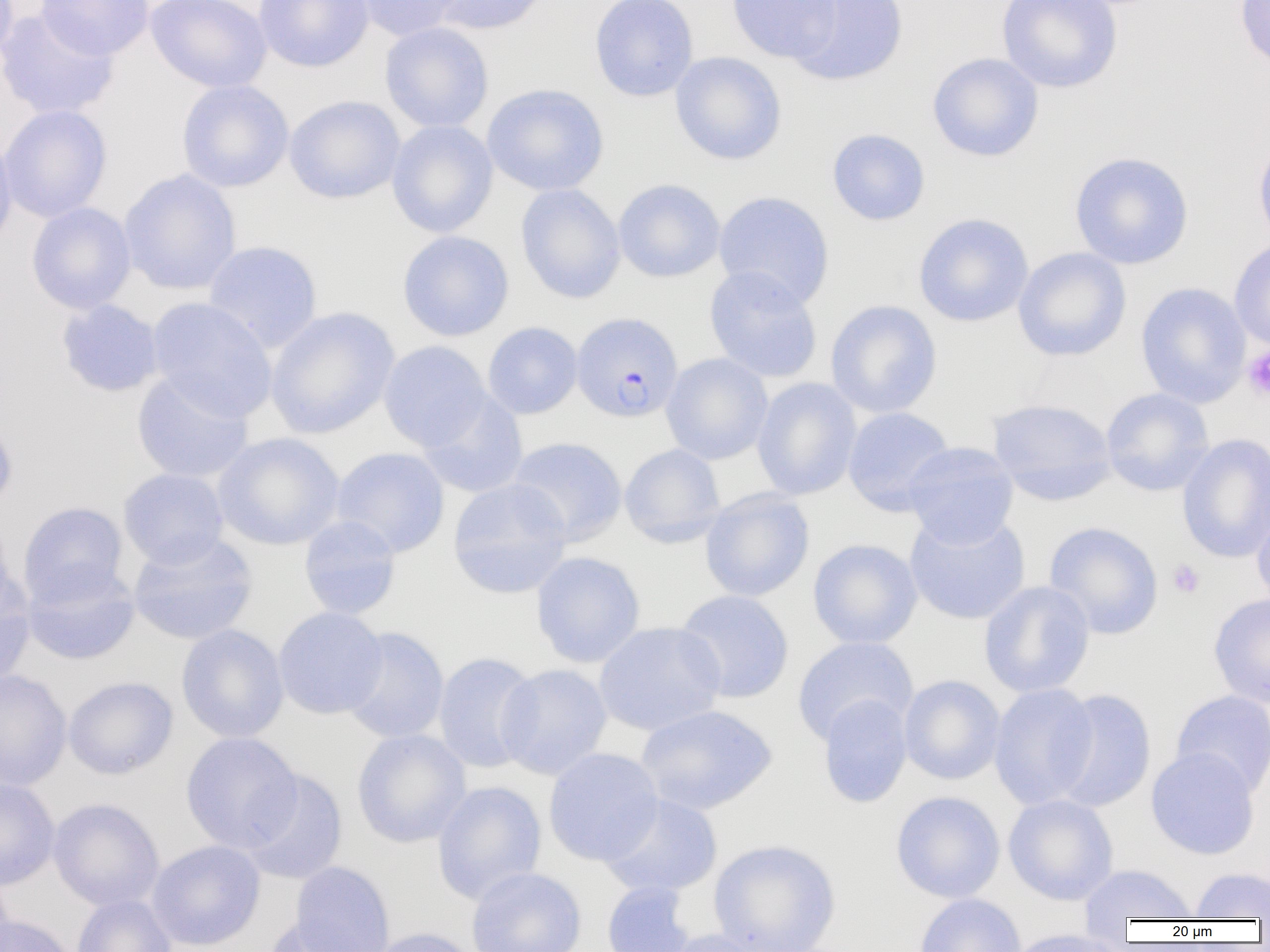
Summary:
  - Coordinate format: approximate bounding boxes as (x1, y1, x2, y2) in pixels
  - Plasmodium falciparum-infected red blood cell locations: (571, 312, 683, 422)
  - Uninfected red blood cell locations: (0, 0, 19, 72), (36, 0, 154, 60), (146, 0, 272, 92), (254, 0, 374, 72), (350, 0, 466, 41), (428, 0, 550, 35), (589, 0, 699, 101), (726, 0, 842, 64), (787, 0, 909, 87), (997, 0, 1123, 93), (1235, 0, 1270, 72), (0, 8, 120, 120), (379, 22, 494, 133), (670, 51, 787, 165), (927, 52, 1044, 162), (176, 80, 295, 192), (482, 83, 609, 196), (284, 95, 405, 204), (0, 104, 112, 223), (386, 120, 498, 238), (827, 128, 930, 226), (0, 131, 17, 250), (1253, 135, 1270, 251), (1069, 151, 1193, 269), (119, 169, 241, 296), (613, 179, 726, 283), (516, 183, 626, 304), (713, 190, 835, 308), (26, 202, 136, 314), (913, 213, 1034, 327), (397, 230, 514, 342), (1229, 238, 1270, 351), (202, 240, 323, 353), (1012, 247, 1132, 361), (704, 265, 823, 383), (1135, 281, 1252, 408), (146, 297, 277, 421), (56, 299, 164, 397), (825, 299, 943, 418), (265, 306, 400, 439), (482, 322, 583, 419), (378, 340, 492, 452), (661, 353, 773, 465), (131, 370, 254, 483), (752, 378, 862, 500), (1100, 387, 1214, 496), (416, 390, 529, 498), (987, 398, 1117, 505), (842, 407, 956, 516), (0, 414, 18, 514), (212, 432, 345, 550), (1176, 433, 1270, 563), (506, 436, 628, 546), (902, 442, 1019, 548), (619, 443, 726, 548), (330, 446, 450, 558), (118, 468, 229, 569), (447, 478, 572, 599), (699, 487, 815, 602), (17, 501, 130, 606), (1252, 503, 1270, 612), (904, 511, 1031, 625), (0, 515, 15, 620), (298, 515, 402, 620), (1043, 521, 1164, 640), (127, 531, 258, 646), (807, 538, 923, 649), (531, 551, 646, 668), (22, 563, 140, 665), (0, 572, 35, 687), (978, 580, 1096, 698), (673, 589, 795, 703), (1208, 593, 1270, 707), (273, 606, 388, 719), (594, 621, 726, 735), (176, 624, 289, 743), (340, 626, 450, 744), (791, 636, 919, 745), (433, 651, 541, 773), (496, 663, 612, 780), (0, 670, 72, 790), (898, 674, 1005, 785), (63, 676, 178, 780), (989, 682, 1099, 809), (1050, 688, 1157, 812), (1170, 689, 1270, 797), (817, 693, 913, 808), (635, 704, 777, 815), (351, 729, 471, 848), (180, 731, 302, 853), (542, 747, 663, 866), (1145, 747, 1260, 860), (239, 768, 348, 885), (0, 776, 60, 891), (432, 780, 547, 905), (890, 790, 1006, 902), (599, 793, 723, 898), (1003, 794, 1119, 905), (48, 798, 164, 911), (707, 838, 842, 952), (146, 840, 266, 951), (288, 861, 395, 952), (1078, 864, 1197, 923), (466, 866, 587, 952), (1189, 867, 1269, 919), (0, 871, 15, 952), (601, 881, 696, 952), (914, 893, 1027, 952), (71, 895, 177, 952), (0, 914, 78, 952), (263, 919, 365, 952), (367, 927, 481, 952), (659, 928, 777, 952), (1003, 929, 1134, 952)
  - Platelet locations: (1242, 346, 1270, 401), (1167, 559, 1205, 599)
  - Slide-level diagnosis: Plasmodium falciparum
  - Image size: 1270×952 pixels
  - Magnification: 1000x
  - Modality: optical microscopy
  - Preparation: thin blood film
  - Field of view: one of a larger specimen